Report the malaria status of this cell.
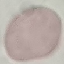

Uninfected.

Summary:
  - Stain: Giemsa
  - Preparation: thin blood smear
  - Capture: smartphone through the microscope eyepiece
  - Image type: cell patch, automatically extracted from a larger field of view and resized to 64 × 64 pixels